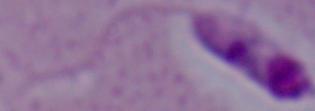 Micrograph. A Leishmania parasite is shown. 1000x magnification.